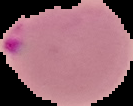

Summary:
  - Image type: cell region segmented out of the field of view; surrounding area masked to black
  - Image size: 133×106 pixels
  - Malaria status: parasitized
  - Preparation: thin blood film